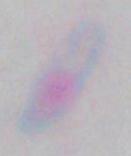
1000x magnification. Toxoplasma gondii is shown. Micrograph.